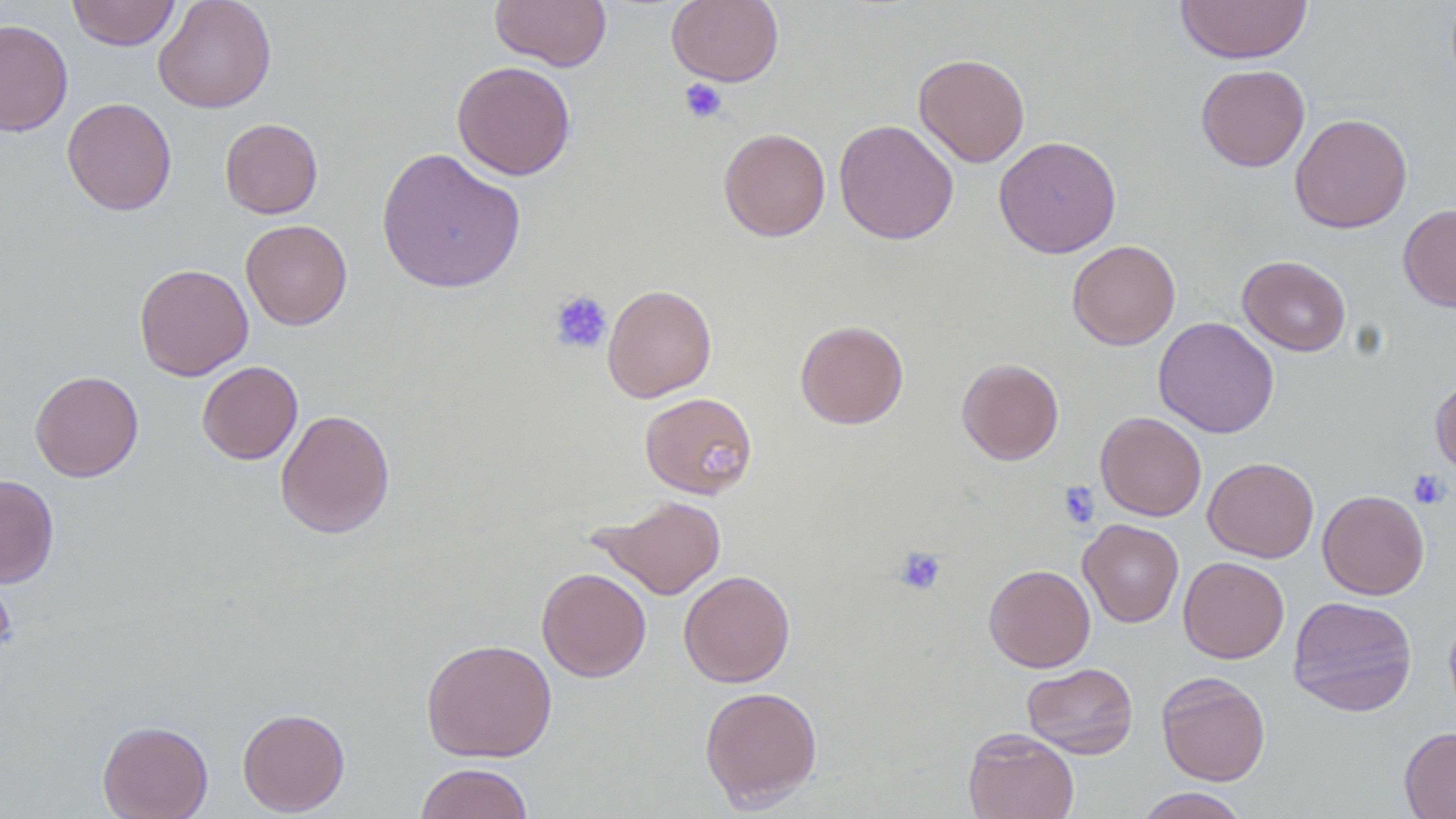
Approximate bounding boxes as (x1, y1, x2, y2) in pixels. Uninfected red blood cell locations: (67, 0, 180, 50), (153, 0, 276, 113), (490, 0, 612, 71), (666, 0, 784, 87), (1175, 0, 1312, 65), (0, 19, 73, 136), (914, 53, 1030, 167), (451, 61, 576, 180), (1196, 64, 1310, 172), (61, 96, 177, 215), (1290, 113, 1412, 234), (220, 118, 323, 219), (834, 119, 959, 244), (718, 126, 831, 241), (994, 136, 1122, 258), (376, 147, 526, 294), (1398, 203, 1456, 312), (241, 219, 352, 330), (1067, 240, 1180, 350), (1237, 255, 1351, 356), (134, 263, 253, 380), (602, 284, 716, 402), (1153, 317, 1279, 438), (794, 320, 909, 429), (957, 357, 1064, 465), (197, 361, 303, 464), (30, 370, 144, 482), (1430, 375, 1456, 477), (639, 392, 758, 499), (275, 409, 395, 539), (1095, 412, 1206, 521), (1203, 456, 1319, 562), (0, 474, 59, 587), (1318, 490, 1429, 600), (594, 495, 727, 600), (1078, 519, 1184, 627), (1178, 557, 1289, 663), (984, 564, 1096, 672), (537, 568, 651, 682), (679, 569, 795, 688), (1288, 595, 1417, 717), (422, 638, 558, 762), (1022, 662, 1138, 759), (1156, 671, 1271, 786), (699, 685, 823, 810), (237, 708, 350, 815), (98, 720, 213, 819), (963, 727, 1079, 819), (1399, 727, 1456, 818), (415, 762, 535, 819), (1134, 787, 1249, 819). Platelet locations: (679, 78, 728, 124), (549, 290, 613, 354), (702, 436, 752, 484), (1408, 469, 1450, 510), (1057, 481, 1100, 528), (893, 546, 947, 596). Slide-level diagnosis: negative for blood parasites. Single field of view. Thin blood film. Image is 1456×819 pixels. Captured at 1000x magnification. Light microscopy.